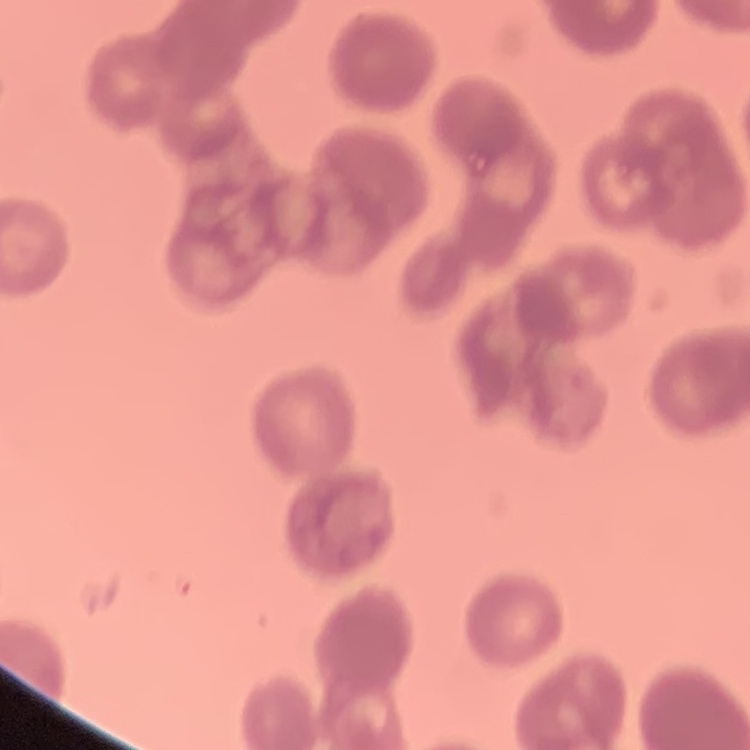
The red blood cells exhibit rouleaux formation. One tile cut from a larger photomicrograph. Stained with either Field's or Giemsa. Thin peripheral smear.